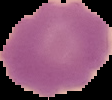

preparation: thin blood smear
result: negative for malaria parasites
image_type: cell region segmented out of the field of view; surrounding area masked to black
image_size: 112×100 pixels